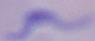
Summary:
  - Magnification: 1000x
  - Identification: trypanosome
  - Modality: micrograph